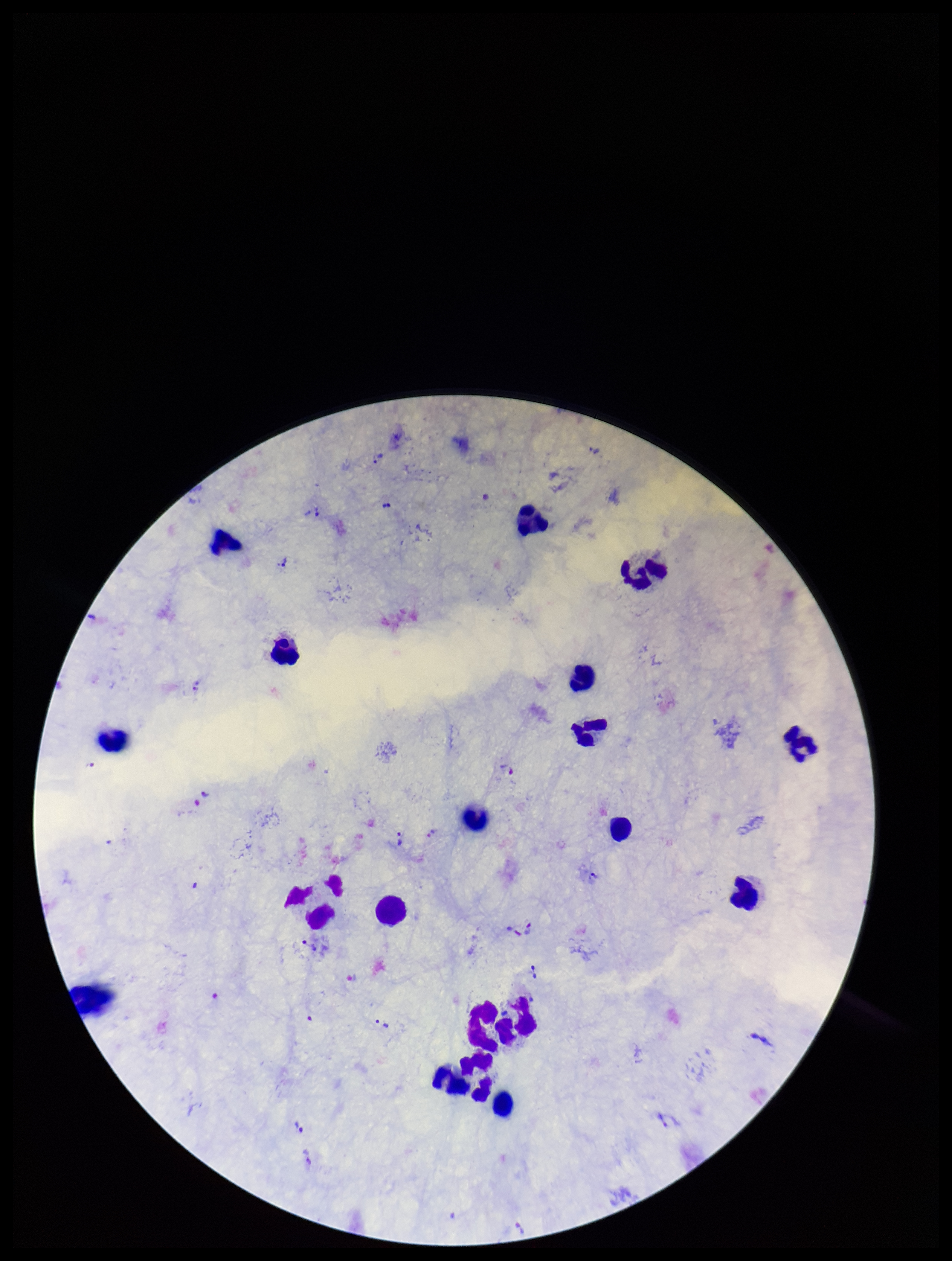

{
  "field_of_view": "one from this slide",
  "patient_malaria_status": "positive",
  "stain": "Giemsa",
  "image_size": "952×1261 pixels",
  "preparation": "thick blood smear",
  "plasmodium_parasites": "seen",
  "leukocyte_count": 18,
  "parasite_count": 19,
  "capture": "smartphone photograph through the microscope eyepiece",
  "species_reported_for_this_patient": "Plasmodium vivax"
}